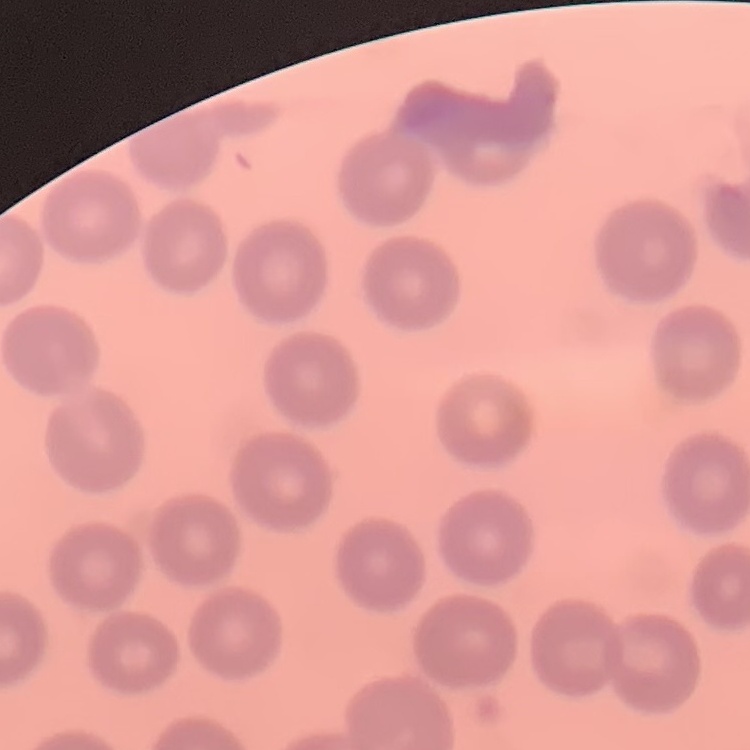 The red blood cells show no rouleaux formation. One tile cut from a larger photomicrograph. Thin blood film. Field's or Giemsa stain.